Assess the morphology of the erythrocytes.
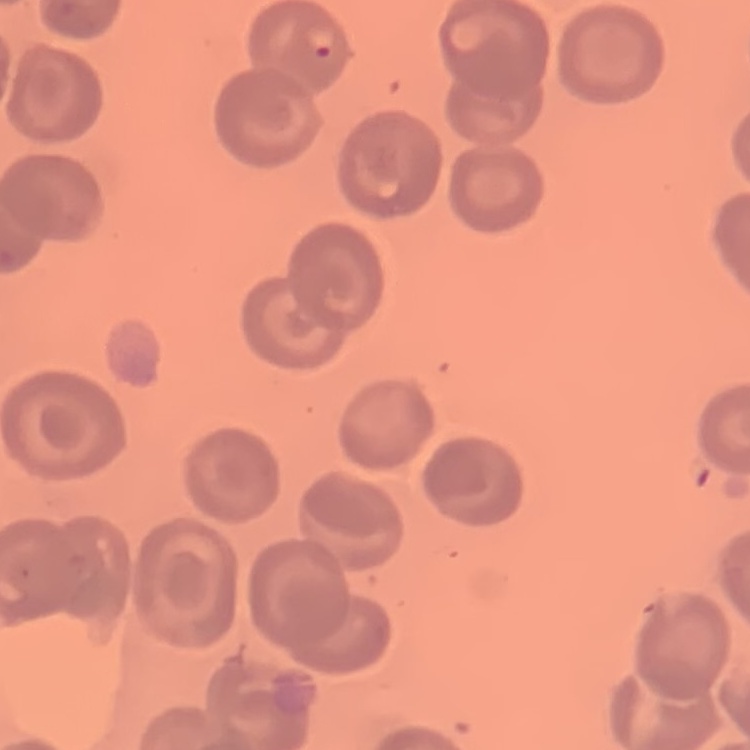

No rouleaux formation.

Summary:
  - Stain: Field's or Giemsa
  - Image type: one tile cut from a larger photomicrograph
  - Preparation: thin peripheral smear